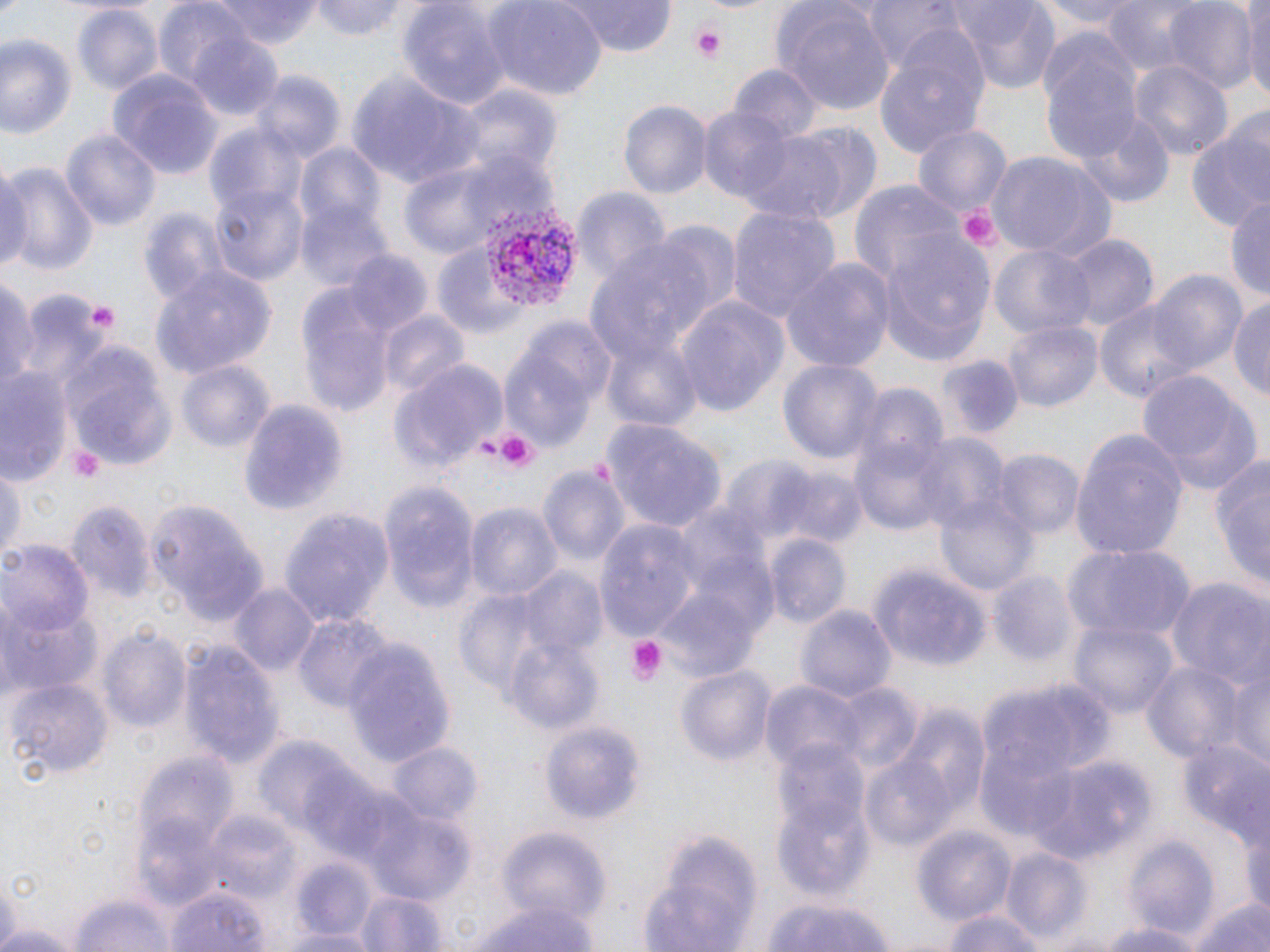

{
  "slide_level_diagnosis": "Plasmodium vivax",
  "image_size": "1270×952 pixels",
  "stain": "May-Grünwald-Giemsa",
  "field_of_view": "one of a larger specimen",
  "preparation": "thin blood smear",
  "uninfected_red_blood_cell_locations": "approximate bounding boxes as [x1, y1, x2, y2] in pixels: [211, 0, 319, 47], [313, 0, 414, 41], [483, 0, 607, 99], [561, 0, 681, 57], [862, 0, 962, 73], [947, 0, 1063, 92], [1040, 0, 1148, 35], [1101, 0, 1201, 74], [1164, 0, 1259, 93], [398, 1, 509, 115], [775, 1, 896, 119], [152, 2, 254, 88], [1243, 3, 1269, 101], [71, 5, 163, 97], [182, 27, 286, 123], [874, 29, 989, 159], [0, 31, 78, 141], [1039, 31, 1143, 164], [729, 60, 823, 143], [1132, 60, 1233, 163], [108, 67, 222, 182], [346, 69, 478, 193], [251, 71, 343, 165], [444, 82, 563, 182], [619, 98, 712, 200], [697, 106, 801, 206], [1071, 114, 1175, 207], [1186, 118, 1269, 232], [205, 119, 307, 218], [742, 124, 875, 220], [911, 125, 1010, 215], [62, 129, 163, 234], [295, 143, 387, 234], [985, 152, 1116, 261], [397, 154, 540, 258], [0, 158, 30, 279], [0, 160, 97, 274], [849, 180, 961, 287], [210, 183, 309, 287], [575, 188, 671, 284], [1226, 194, 1270, 302], [296, 200, 394, 292], [727, 204, 841, 325], [136, 208, 230, 310], [877, 229, 997, 371], [1060, 235, 1157, 333], [432, 242, 532, 341], [991, 243, 1095, 344], [344, 253, 430, 338], [782, 256, 894, 372], [151, 267, 276, 379], [1146, 268, 1249, 378], [1, 276, 37, 397], [297, 291, 397, 420], [24, 294, 110, 379], [676, 295, 791, 416], [1231, 295, 1270, 401], [1096, 302, 1202, 407], [379, 312, 468, 399], [1003, 318, 1103, 412], [64, 346, 171, 467], [500, 351, 599, 455], [932, 351, 1023, 442], [780, 357, 882, 468], [176, 359, 275, 457], [388, 359, 508, 472], [0, 368, 75, 485], [1137, 369, 1263, 496], [853, 385, 947, 475], [238, 396, 348, 520], [599, 416, 726, 536], [1073, 431, 1189, 559], [851, 434, 950, 539], [915, 435, 1011, 541], [1209, 450, 1270, 595], [992, 451, 1082, 540], [719, 456, 821, 545], [772, 463, 870, 548], [539, 465, 630, 571], [0, 471, 23, 559], [378, 484, 479, 612], [936, 496, 1038, 597], [66, 500, 155, 601], [151, 500, 268, 625], [467, 503, 561, 605], [280, 511, 392, 627], [595, 520, 702, 641], [766, 536, 849, 628], [2, 543, 92, 635], [1063, 543, 1195, 642], [868, 562, 991, 674], [519, 569, 610, 663], [988, 572, 1078, 669], [1166, 580, 1270, 687], [231, 585, 320, 678], [454, 589, 554, 699], [2, 602, 101, 700], [796, 603, 898, 705], [293, 612, 394, 716], [1067, 616, 1181, 719], [100, 626, 192, 735], [502, 636, 603, 732], [182, 639, 282, 771], [343, 643, 455, 766], [1139, 660, 1247, 770], [1225, 663, 1269, 776], [676, 666, 775, 767], [978, 675, 1117, 792], [7, 676, 113, 778], [762, 681, 867, 772], [832, 683, 922, 772], [892, 705, 989, 826], [539, 717, 649, 832], [1174, 737, 1266, 841], [255, 739, 364, 839], [388, 742, 484, 826], [132, 750, 237, 858], [1022, 754, 1153, 862], [863, 757, 956, 849], [773, 776, 875, 901], [363, 803, 475, 903], [203, 808, 299, 903], [1240, 808, 1270, 918], [136, 819, 229, 910], [912, 826, 1016, 928], [495, 828, 610, 931], [638, 828, 764, 951], [1125, 837, 1220, 938], [1001, 847, 1090, 944], [293, 860, 378, 941], [169, 883, 272, 952], [357, 887, 448, 952], [66, 888, 178, 952], [1180, 891, 1270, 952], [470, 897, 597, 952], [753, 897, 901, 951], [941, 908, 1049, 952], [1093, 919, 1205, 952], [280, 927, 380, 952]",
  "platelet_locations": "approximate bounding boxes as [x1, y1, x2, y2] in pixels: [688, 20, 729, 63], [953, 205, 1003, 253], [88, 303, 116, 329], [476, 428, 541, 476], [68, 445, 105, 483], [624, 635, 670, 686]",
  "magnification": "1000x",
  "modality": "light microscopy",
  "plasmodium_vivax_infected_red_blood_cell_locations": "approximate bounding boxes as [x1, y1, x2, y2] in pixels: [480, 207, 577, 307]"
}